Describe the morphology of the red blood cells.
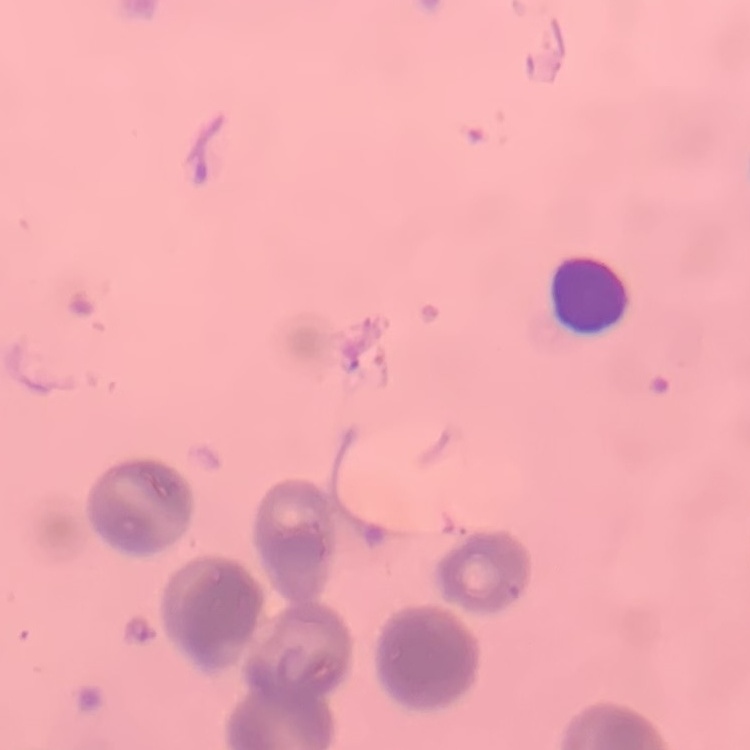
They show rouleaux formation.

Summary:
  - Preparation: thin blood smear
  - Image type: one tile cut from a larger photomicrograph
  - Stain: Field's or Giemsa